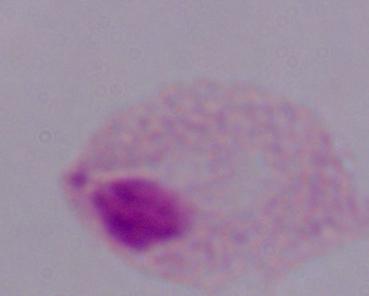
Summary:
  - Magnification: 1000x
  - Identification: trichomonad
  - Modality: photomicrograph